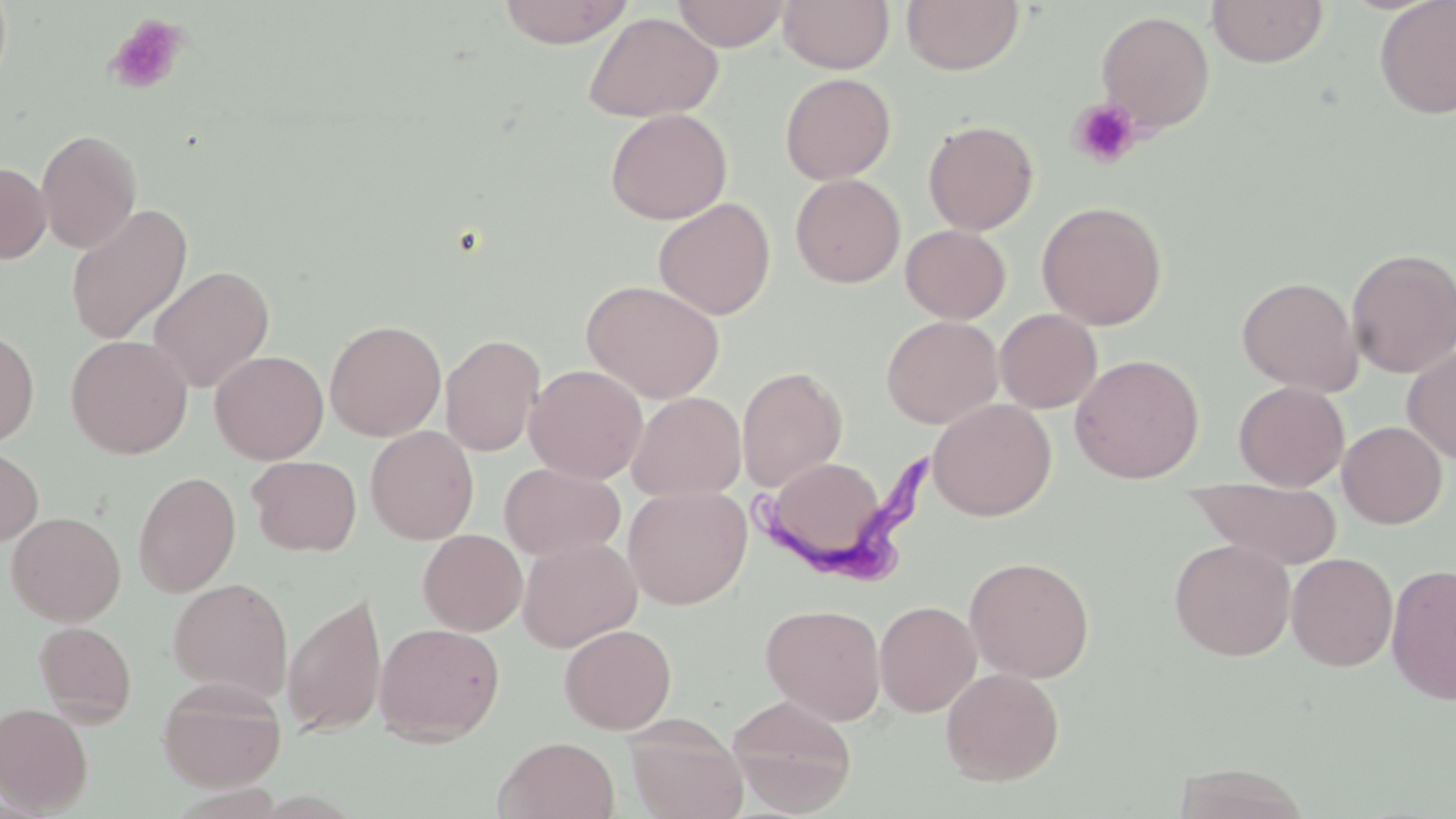
Approximate bounding boxes as named x1/y1/x2/y2 corners in pixels. Uninfected red blood cell locations: (x1=497, y1=0, x2=634, y2=48), (x1=671, y1=0, x2=791, y2=51), (x1=778, y1=0, x2=894, y2=73), (x1=901, y1=0, x2=1024, y2=75), (x1=1374, y1=0, x2=1456, y2=120), (x1=1206, y1=1, x2=1329, y2=68), (x1=1096, y1=10, x2=1215, y2=135), (x1=583, y1=12, x2=723, y2=123), (x1=779, y1=72, x2=896, y2=185), (x1=605, y1=108, x2=732, y2=224), (x1=922, y1=120, x2=1039, y2=235), (x1=36, y1=128, x2=142, y2=254), (x1=0, y1=161, x2=51, y2=263), (x1=790, y1=174, x2=906, y2=288), (x1=653, y1=197, x2=776, y2=320), (x1=1036, y1=200, x2=1168, y2=330), (x1=65, y1=203, x2=192, y2=345), (x1=900, y1=225, x2=1011, y2=323), (x1=1346, y1=248, x2=1456, y2=378), (x1=148, y1=265, x2=275, y2=393), (x1=1237, y1=276, x2=1362, y2=396), (x1=582, y1=279, x2=725, y2=403), (x1=994, y1=308, x2=1102, y2=413), (x1=881, y1=315, x2=1003, y2=428), (x1=324, y1=319, x2=446, y2=442), (x1=0, y1=327, x2=39, y2=449), (x1=440, y1=333, x2=546, y2=457), (x1=65, y1=335, x2=192, y2=459), (x1=1401, y1=343, x2=1456, y2=465), (x1=209, y1=350, x2=329, y2=464), (x1=1069, y1=354, x2=1204, y2=483), (x1=524, y1=364, x2=648, y2=484), (x1=736, y1=366, x2=848, y2=491), (x1=1233, y1=381, x2=1349, y2=491), (x1=627, y1=391, x2=746, y2=501), (x1=928, y1=398, x2=1057, y2=520), (x1=1337, y1=421, x2=1448, y2=529), (x1=365, y1=425, x2=479, y2=544), (x1=0, y1=445, x2=43, y2=547), (x1=247, y1=455, x2=362, y2=556), (x1=772, y1=460, x2=887, y2=550), (x1=499, y1=462, x2=625, y2=561), (x1=133, y1=470, x2=241, y2=597), (x1=1188, y1=478, x2=1343, y2=569), (x1=623, y1=485, x2=752, y2=609), (x1=6, y1=511, x2=126, y2=625), (x1=418, y1=529, x2=527, y2=635), (x1=518, y1=536, x2=641, y2=651), (x1=1169, y1=538, x2=1295, y2=661), (x1=1286, y1=552, x2=1398, y2=671), (x1=964, y1=555, x2=1095, y2=683), (x1=1386, y1=562, x2=1456, y2=704), (x1=168, y1=578, x2=293, y2=702), (x1=282, y1=591, x2=387, y2=738), (x1=874, y1=600, x2=981, y2=717), (x1=760, y1=604, x2=886, y2=725), (x1=33, y1=621, x2=136, y2=724), (x1=374, y1=622, x2=505, y2=744), (x1=559, y1=623, x2=676, y2=734), (x1=940, y1=667, x2=1065, y2=786), (x1=157, y1=676, x2=286, y2=791), (x1=726, y1=695, x2=857, y2=815), (x1=0, y1=702, x2=94, y2=814), (x1=625, y1=716, x2=748, y2=819), (x1=494, y1=736, x2=620, y2=819), (x1=1173, y1=763, x2=1312, y2=819). Trypanosoma brucei locations: (x1=752, y1=454, x2=932, y2=584). Platelet locations: (x1=104, y1=13, x2=189, y2=95), (x1=1068, y1=98, x2=1141, y2=169). Slide-level diagnosis: Trypanosoma brucei. Optical microscopy. Image is 1456×819 pixels. Thin blood smear. One field of a larger specimen. 1000x magnification. May-Grünwald-Giemsa stain.